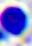

identification: leukocyte
magnification: 400x
modality: micrograph